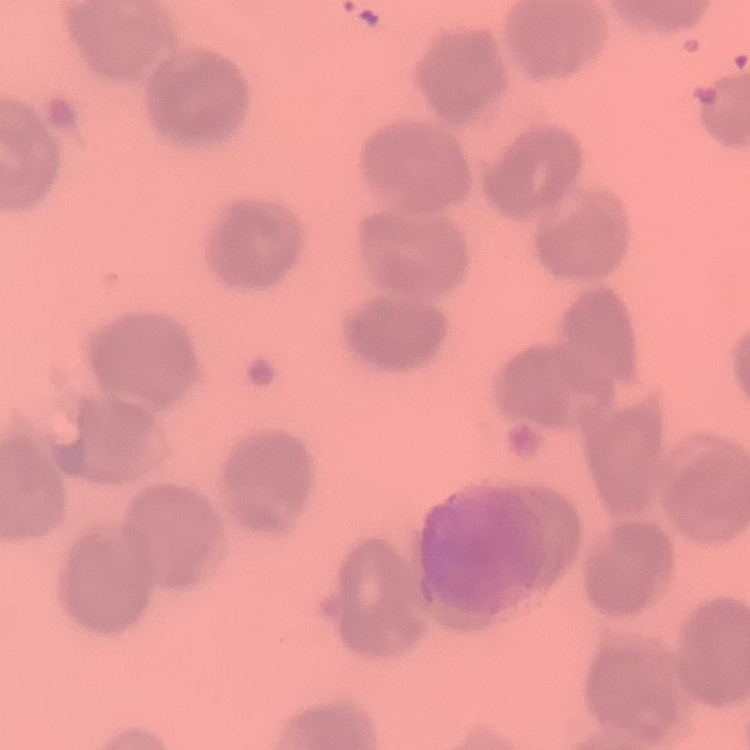
Summary:
  - Red blood cell morphology: no rouleaux formation
  - Preparation: thin blood smear
  - Image type: one tile cut from a larger photomicrograph
  - Stain: Field's or Giemsa